Comment on the morphology of the erythrocytes.
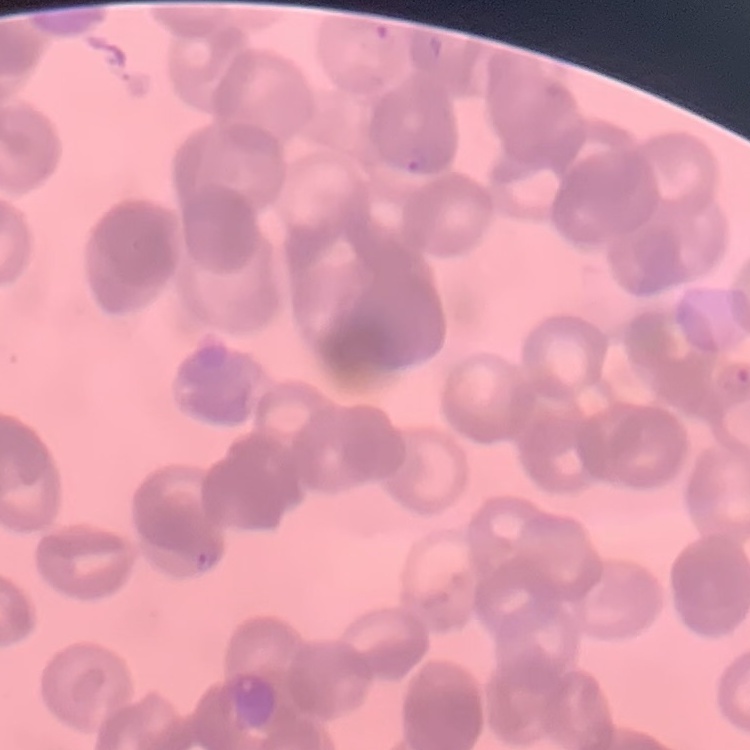
They show rouleaux formation.

Thin peripheral smear. Field's or Giemsa stain. Square crop of a larger photomicrograph.